Evaluate for parasitized red blood cells.
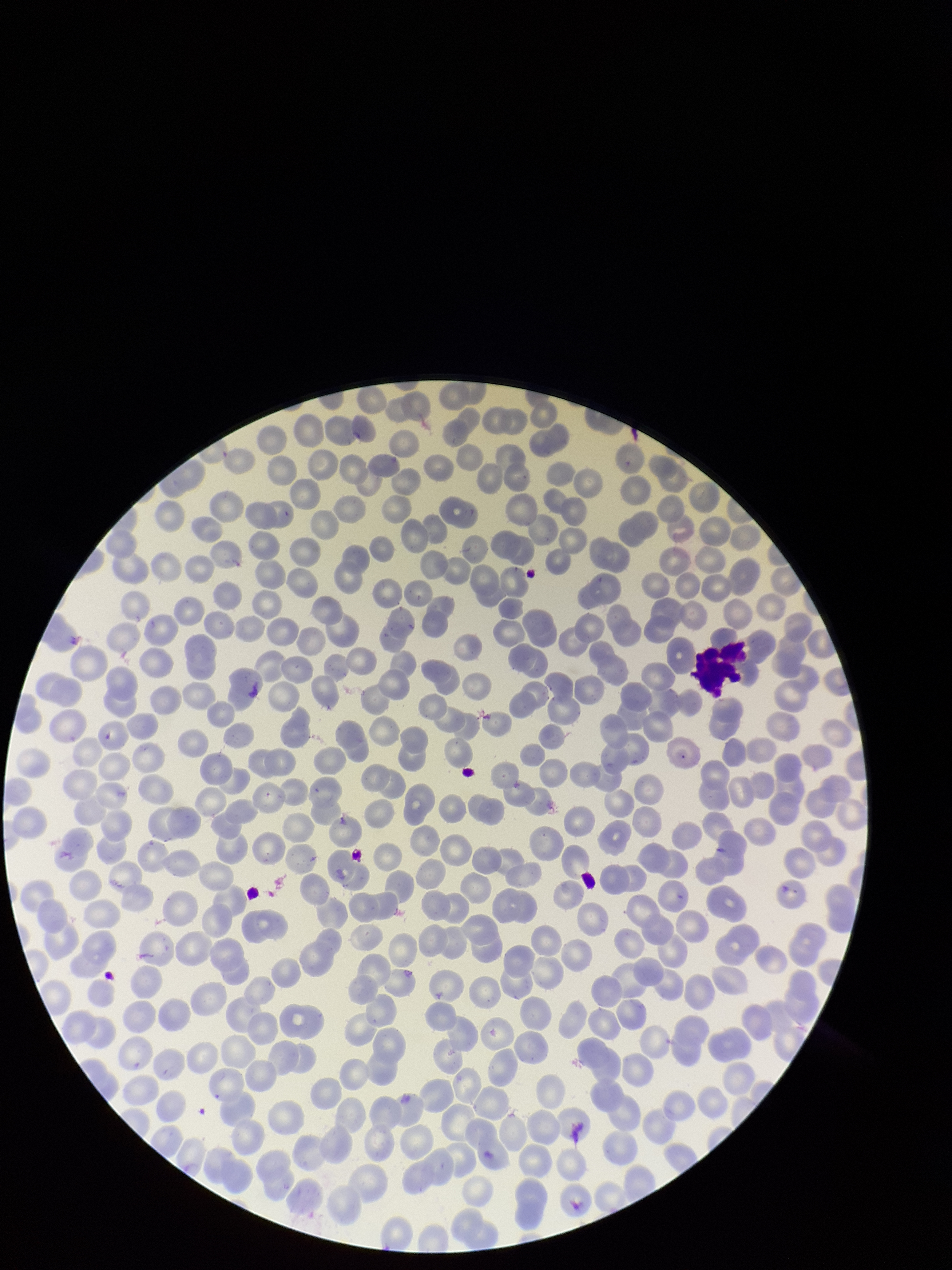

None seen.

Single field of view. Patient malaria status: infected. Stained with Giemsa. Smartphone photograph taken through the eyepiece of a microscope. Parasitized red blood cell count: 0. Species reported for this patient: Plasmodium vivax. Image is 952×1270 pixels. Preparation: thin blood smear. Red blood cell count: 267.